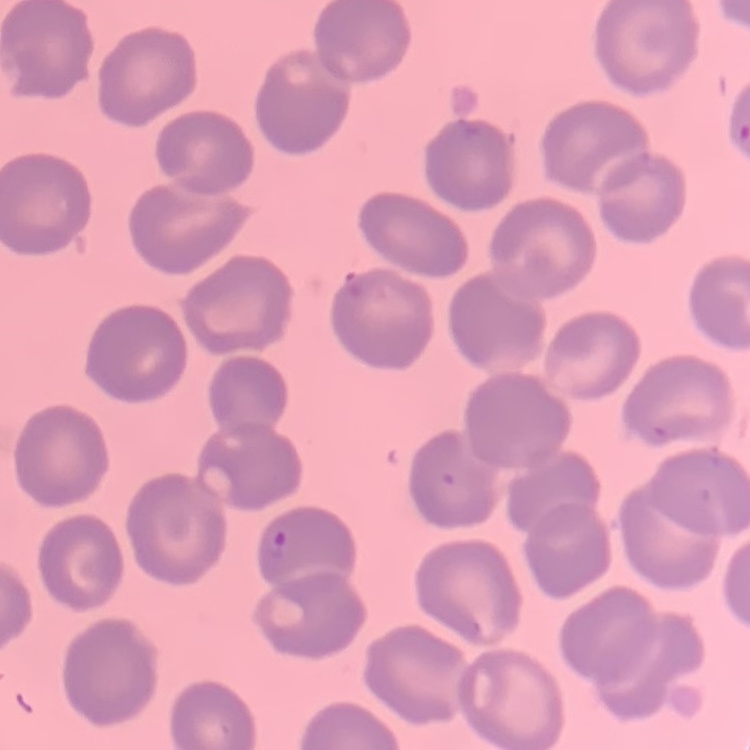

Summary:
  - Red blood cell morphology: no rouleaux formation
  - Image type: one tile cut from a larger photomicrograph
  - Preparation: thin peripheral smear
  - Stain: Field's or Giemsa